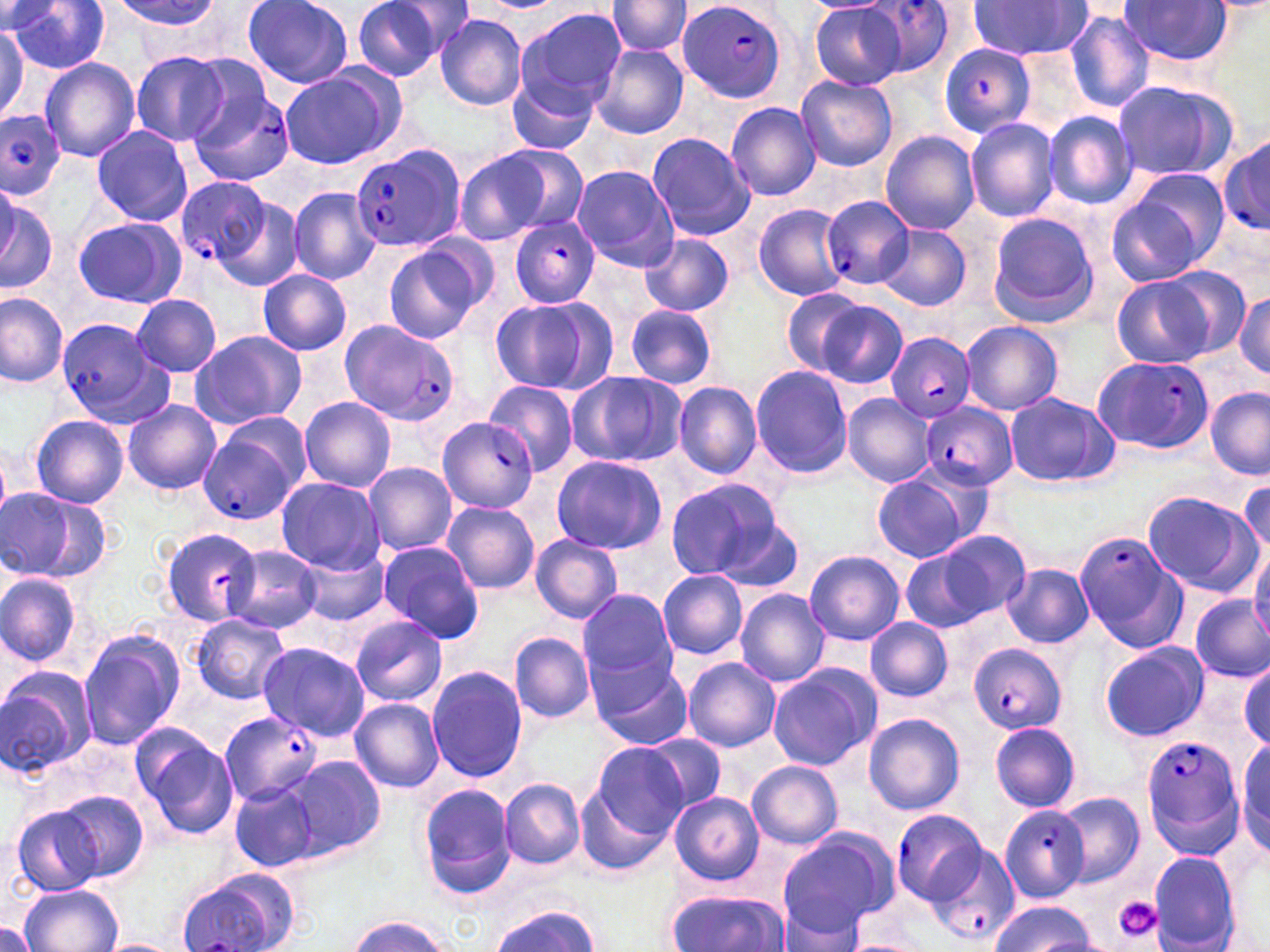
Summary:
  - Coordinate format: approximate bounding boxes as (x1, y1, x2, y2) in pixels
  - Platelet locations: (1114, 896, 1161, 941)
  - Uninfected red blood cell locations: (241, 0, 352, 89), (353, 0, 449, 81), (386, 0, 479, 59), (1120, 0, 1234, 66), (9, 1, 110, 74), (112, 1, 224, 31), (607, 1, 692, 59), (966, 1, 1093, 60), (810, 3, 906, 89), (516, 7, 626, 111), (1064, 10, 1154, 114), (435, 14, 527, 111), (0, 16, 37, 120), (591, 45, 689, 139), (132, 51, 231, 145), (39, 58, 140, 161), (279, 71, 395, 167), (507, 72, 597, 156), (795, 75, 898, 172), (1112, 80, 1238, 183), (726, 101, 821, 201), (1044, 111, 1136, 210), (964, 117, 1059, 223), (91, 127, 193, 227), (881, 131, 980, 235), (646, 132, 755, 240), (492, 145, 589, 233), (454, 150, 557, 246), (570, 165, 679, 272), (1105, 185, 1222, 287), (288, 186, 380, 285), (0, 192, 57, 294), (201, 192, 305, 294), (753, 203, 849, 301), (985, 212, 1100, 326), (73, 216, 188, 308), (880, 224, 972, 310), (640, 234, 734, 316), (386, 243, 486, 343), (257, 270, 351, 356), (1111, 274, 1225, 369), (777, 290, 874, 378), (1234, 290, 1269, 376), (0, 291, 69, 387), (132, 294, 221, 377), (487, 296, 611, 396), (810, 298, 908, 389), (624, 304, 718, 390), (960, 320, 1065, 416), (189, 329, 307, 430), (751, 364, 854, 479), (565, 370, 687, 468), (484, 381, 577, 479), (673, 381, 762, 479), (1206, 389, 1270, 479), (1004, 393, 1118, 488), (841, 394, 935, 488), (298, 397, 397, 491), (123, 399, 222, 495), (30, 414, 129, 509), (550, 455, 668, 555), (361, 461, 458, 554), (870, 472, 977, 562), (1239, 475, 1269, 566), (276, 476, 384, 573), (663, 476, 789, 584), (1, 489, 76, 579), (1141, 489, 1262, 596), (442, 502, 539, 594), (161, 525, 264, 627), (901, 531, 1030, 632), (530, 534, 623, 623), (378, 541, 485, 643), (295, 543, 387, 628), (1250, 545, 1270, 642), (223, 546, 323, 633), (803, 550, 905, 646), (1003, 565, 1095, 648), (658, 570, 748, 659), (0, 572, 83, 669), (734, 588, 831, 687), (578, 589, 676, 684), (1190, 596, 1269, 683), (189, 615, 290, 703), (865, 617, 952, 701), (349, 618, 446, 707), (76, 629, 186, 752), (509, 630, 595, 723), (257, 641, 369, 741), (1098, 641, 1207, 740), (682, 656, 781, 753), (588, 657, 693, 751), (1236, 662, 1268, 750), (766, 665, 881, 771), (0, 666, 96, 779), (426, 666, 528, 783), (350, 699, 444, 793), (863, 711, 965, 816), (990, 721, 1082, 812), (131, 724, 239, 840), (642, 734, 728, 813), (1235, 737, 1269, 858), (593, 743, 688, 837), (285, 757, 385, 861), (747, 761, 844, 849), (499, 779, 586, 870), (230, 782, 318, 872), (418, 783, 513, 900), (573, 783, 675, 879), (49, 788, 150, 885), (1055, 791, 1144, 886), (670, 792, 764, 885), (11, 804, 107, 895), (776, 828, 897, 936), (1147, 851, 1241, 950), (17, 882, 125, 952), (662, 888, 788, 952), (774, 899, 865, 952), (993, 899, 1093, 951), (490, 904, 601, 952), (350, 916, 452, 951), (0, 919, 39, 951), (838, 937, 930, 952), (95, 938, 182, 952)
  - Plasmodium falciparum-infected red blood cell locations: (864, 0, 954, 78), (677, 1, 788, 102), (937, 45, 1035, 140), (188, 84, 294, 187), (0, 110, 67, 199), (1219, 135, 1270, 238), (350, 145, 464, 253), (174, 177, 277, 275), (823, 196, 913, 293), (509, 217, 601, 308), (57, 318, 175, 431), (341, 318, 457, 429), (885, 333, 976, 422), (1092, 354, 1214, 455), (919, 401, 1017, 491), (435, 415, 537, 515), (199, 431, 299, 525), (1076, 529, 1185, 651), (969, 642, 1069, 736), (220, 711, 323, 804), (1142, 735, 1241, 852), (998, 803, 1088, 901), (891, 811, 986, 905), (928, 844, 1021, 947), (178, 876, 287, 951)
  - Slide-level diagnosis: Plasmodium falciparum
  - Field of view: one of a larger specimen
  - Modality: light microscopy
  - Image size: 1270×952 pixels
  - Magnification: 1000x
  - Stain: May-Grünwald-Giemsa
  - Preparation: thin blood smear